Report the malaria status of this cell.
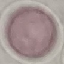
It is uninfected.

Summary:
  - Preparation: thin blood film
  - Capture: smartphone camera at the microscope eyepiece
  - Stain: Giemsa
  - Image type: automatically extracted cell patch, resized to 64 × 64 pixels